Identify the parasite.
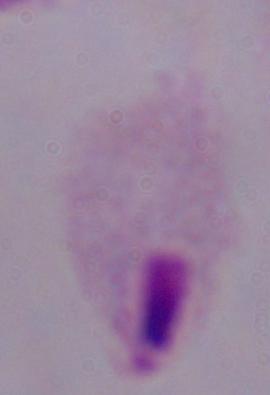

This is a trichomonad.

modality: micrograph
magnification: 1000x